Name the cell type shown.
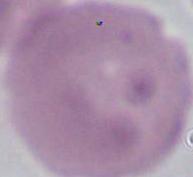
This is an erythrocyte.

Photomicrograph. Captured at 1000x magnification.